Describe the morphology of the erythrocytes.
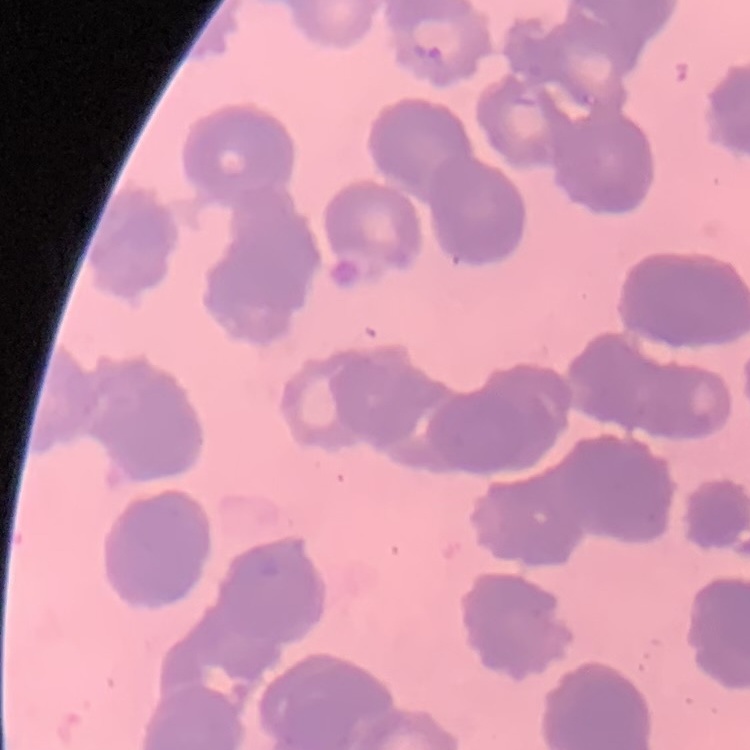

They show rouleaux formation.

Thin peripheral smear. Square crop of a larger photomicrograph. Stained with either Field's or Giemsa.